Describe the morphology of the erythrocytes.
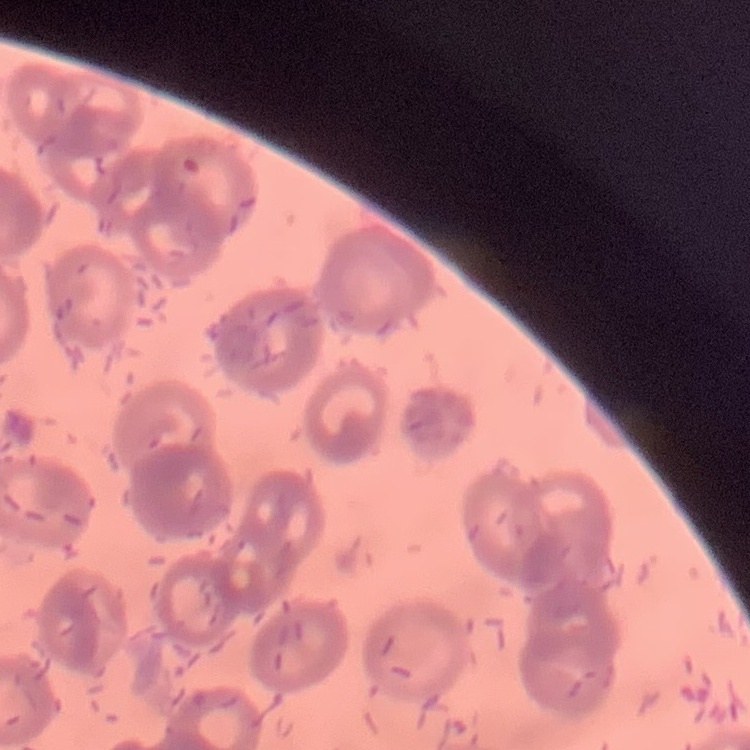
They show rouleaux formation.

{
  "stain": "Field's or Giemsa",
  "image_type": "square crop of a larger photomicrograph",
  "preparation": "thin blood film"
}